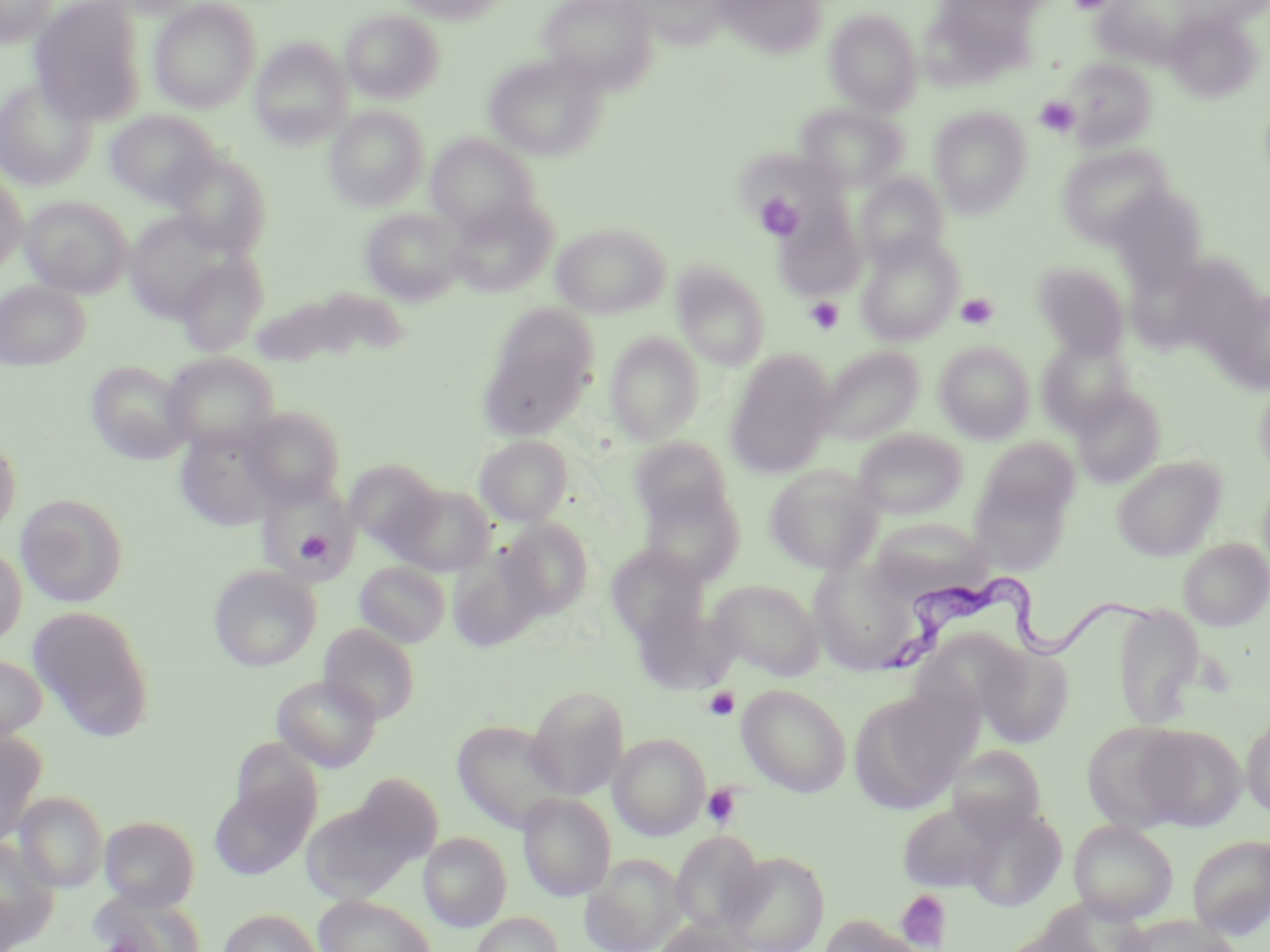
Summary:
  - Coordinate format: approximate bounding boxes as (x1, y1, x2, y2) in pixels
  - Uninfected red blood cell locations: (0, 0, 59, 47), (29, 0, 148, 125), (103, 0, 207, 18), (393, 0, 510, 23), (538, 0, 657, 92), (1092, 0, 1198, 68), (149, 1, 262, 113), (627, 1, 730, 49), (715, 1, 828, 58), (340, 8, 446, 103), (825, 9, 922, 115), (1166, 10, 1261, 102), (249, 39, 353, 148), (483, 53, 609, 161), (1062, 59, 1157, 151), (0, 76, 98, 191), (796, 103, 908, 191), (324, 106, 429, 211), (929, 107, 1032, 217), (105, 109, 220, 207), (425, 134, 539, 234), (1057, 144, 1174, 248), (167, 152, 271, 258), (0, 170, 28, 274), (855, 173, 949, 269), (1108, 184, 1209, 288), (21, 195, 133, 297), (446, 196, 557, 297), (775, 207, 867, 301), (360, 208, 465, 305), (124, 213, 236, 322), (551, 223, 671, 319), (856, 236, 962, 346), (175, 253, 268, 356), (672, 262, 771, 369), (1032, 262, 1130, 359), (0, 280, 91, 370), (248, 289, 388, 367), (1223, 289, 1269, 393), (480, 305, 599, 437), (605, 332, 704, 445), (1036, 337, 1135, 435), (934, 341, 1036, 443), (818, 346, 923, 444), (725, 351, 837, 478), (161, 352, 279, 453), (85, 360, 193, 465), (1255, 373, 1270, 481), (1071, 386, 1165, 487), (238, 406, 346, 508), (174, 425, 284, 531), (853, 428, 968, 518), (0, 433, 21, 539), (474, 435, 573, 526), (629, 437, 735, 529), (979, 437, 1080, 522), (1112, 455, 1226, 561), (343, 460, 443, 554), (764, 464, 882, 573), (968, 476, 1071, 573), (257, 480, 359, 582), (389, 483, 497, 576), (639, 487, 745, 586), (16, 493, 129, 608), (500, 517, 594, 618), (870, 517, 989, 594), (1178, 537, 1270, 630), (0, 544, 27, 646), (606, 544, 710, 643), (447, 546, 545, 652), (354, 561, 451, 647), (809, 561, 920, 674), (208, 565, 321, 671), (707, 579, 826, 680), (1113, 604, 1206, 729), (29, 606, 155, 742), (319, 624, 420, 724), (976, 641, 1074, 747), (0, 654, 47, 743), (272, 674, 381, 772), (737, 683, 852, 797), (526, 686, 629, 800), (847, 687, 970, 815), (1241, 711, 1270, 819), (451, 719, 571, 833), (1081, 721, 1191, 832), (1131, 724, 1247, 830), (0, 730, 47, 845), (609, 734, 710, 840), (229, 740, 321, 831), (946, 743, 1048, 839), (353, 772, 444, 863), (209, 777, 316, 880), (14, 791, 108, 893), (518, 792, 616, 900), (897, 800, 1001, 893), (302, 803, 411, 903), (959, 806, 1068, 911), (99, 816, 200, 910), (1068, 819, 1178, 923), (671, 830, 765, 935), (418, 832, 512, 931), (1187, 835, 1270, 938), (0, 838, 58, 949), (721, 851, 830, 952), (581, 853, 687, 952), (0, 885, 24, 951), (91, 890, 206, 952), (314, 895, 437, 952), (218, 909, 322, 952), (472, 912, 563, 952), (817, 915, 925, 952), (1120, 915, 1240, 952), (653, 920, 755, 952)
  - Platelet locations: (1069, 0, 1114, 14), (1035, 96, 1079, 136), (755, 193, 805, 239), (956, 293, 998, 330), (805, 297, 845, 334), (296, 531, 332, 563), (702, 686, 740, 722), (701, 784, 742, 829), (896, 889, 952, 951), (102, 934, 142, 952)
  - Trypanosoma brucei locations: (881, 566, 1160, 674)
  - Slide-level diagnosis: Trypanosoma brucei
  - Field of view: single
  - Modality: optical microscopy
  - Image size: 1270×952 pixels
  - Preparation: thin blood smear
  - Magnification: 1000x
  - Stain: May-Grünwald-Giemsa